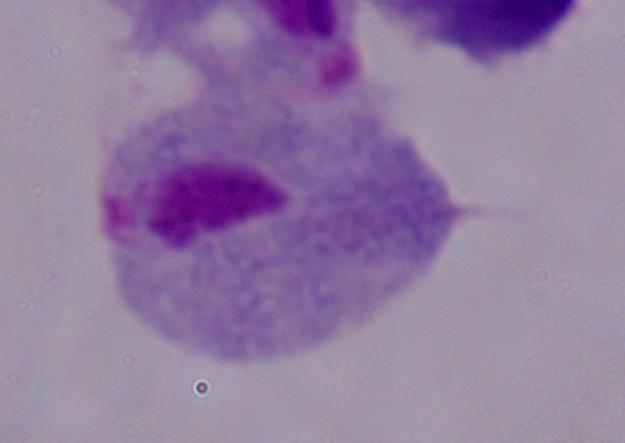 Micrograph. Captured at 1000x magnification. A trichomonad is shown.